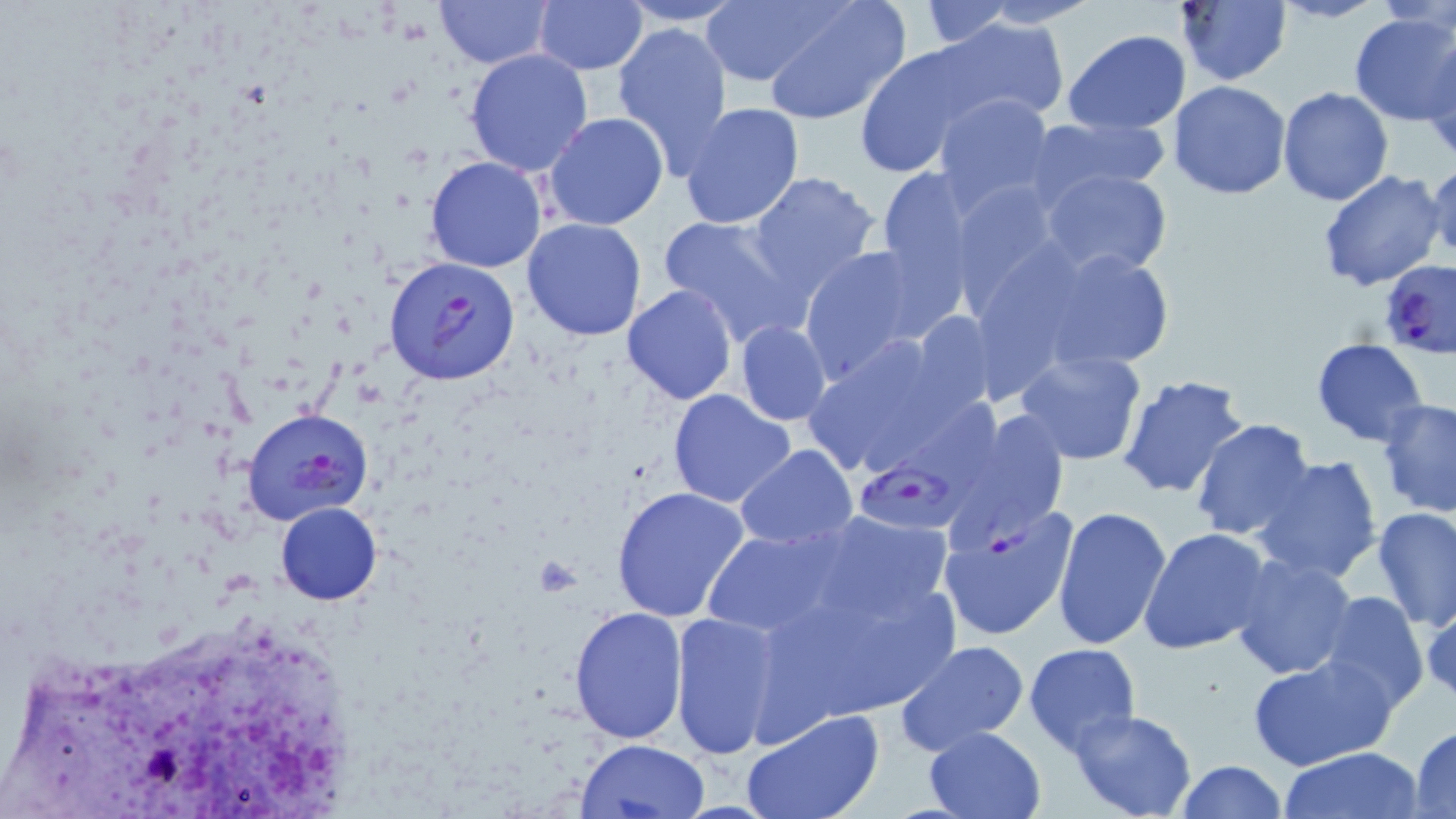
Approximate bounding boxes as [x1, y1, x2, y2] in pixels. Platelet locations: [530, 557, 584, 595]. Plasmodium falciparum-infected red blood cell locations: [384, 254, 522, 385], [1379, 258, 1456, 358], [241, 407, 374, 525], [953, 409, 1070, 557], [853, 458, 965, 537]. Uninfected red blood cell locations: [435, 0, 552, 68], [535, 0, 647, 75], [614, 0, 751, 26], [917, 0, 1015, 48], [969, 0, 1101, 27], [1173, 0, 1292, 86], [697, 1, 836, 88], [1271, 1, 1386, 23], [760, 3, 910, 126], [1347, 12, 1456, 125], [934, 15, 1068, 123], [611, 21, 734, 169], [1064, 29, 1192, 134], [853, 43, 988, 176], [1423, 46, 1456, 165], [465, 47, 595, 177], [1169, 82, 1293, 200], [1278, 86, 1394, 207], [933, 92, 1057, 212], [680, 102, 805, 229], [545, 112, 669, 230], [1028, 115, 1171, 202], [425, 156, 548, 273], [1427, 160, 1455, 266], [874, 165, 978, 300], [1040, 169, 1173, 278], [1317, 170, 1447, 293], [746, 171, 881, 297], [949, 178, 1065, 305], [658, 213, 809, 347], [521, 218, 648, 341], [1004, 237, 1182, 381], [796, 244, 934, 379], [621, 284, 738, 405], [907, 311, 1002, 418], [734, 320, 832, 425], [798, 331, 975, 483], [1310, 339, 1429, 446], [1014, 350, 1147, 465], [1117, 373, 1251, 500], [667, 389, 797, 511], [1375, 398, 1456, 517], [1190, 419, 1317, 541], [735, 446, 858, 547], [1251, 454, 1385, 586], [610, 485, 751, 622], [276, 501, 382, 604], [937, 502, 1078, 642], [1052, 506, 1173, 654], [1372, 507, 1456, 629], [1138, 527, 1273, 655], [702, 528, 848, 640], [753, 532, 970, 724], [1228, 554, 1359, 680], [1317, 591, 1428, 711], [569, 606, 688, 743], [667, 611, 785, 760], [894, 639, 1031, 757], [1024, 643, 1142, 754], [1248, 654, 1398, 771], [739, 707, 887, 819], [1069, 709, 1198, 819], [1408, 724, 1456, 819], [924, 725, 1047, 817], [577, 739, 709, 818], [1277, 746, 1425, 819], [1174, 760, 1289, 818]. Slide-level diagnosis: Plasmodium falciparum. May-Grünwald-Giemsa stain. Single field of view. Captured at 1000x magnification. Thin blood smear. Optical microscopy. Image is 1456×819 pixels.